Name the parasite shown.
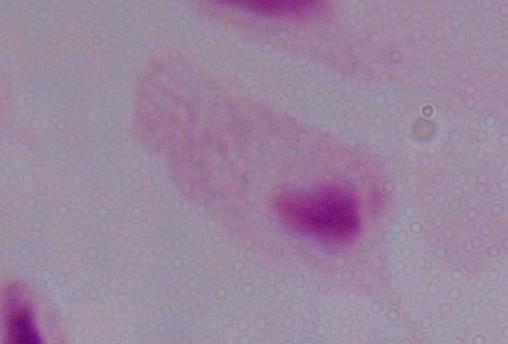
A trichomonad.

magnification = 1000x
modality = micrograph